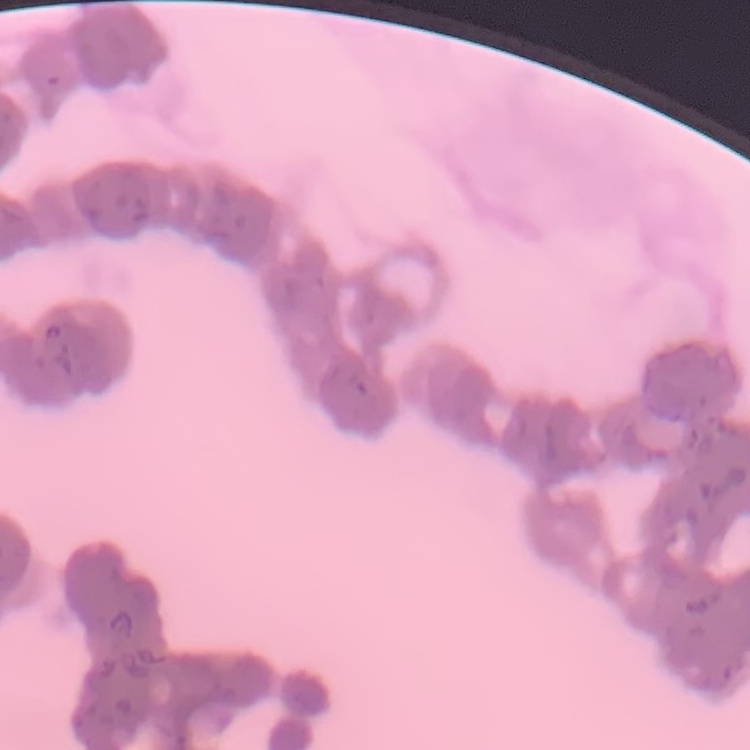

The red blood cells exhibit rouleaux formation. Thin blood film. Square crop of a larger photomicrograph. Stained with either Field's or Giemsa.